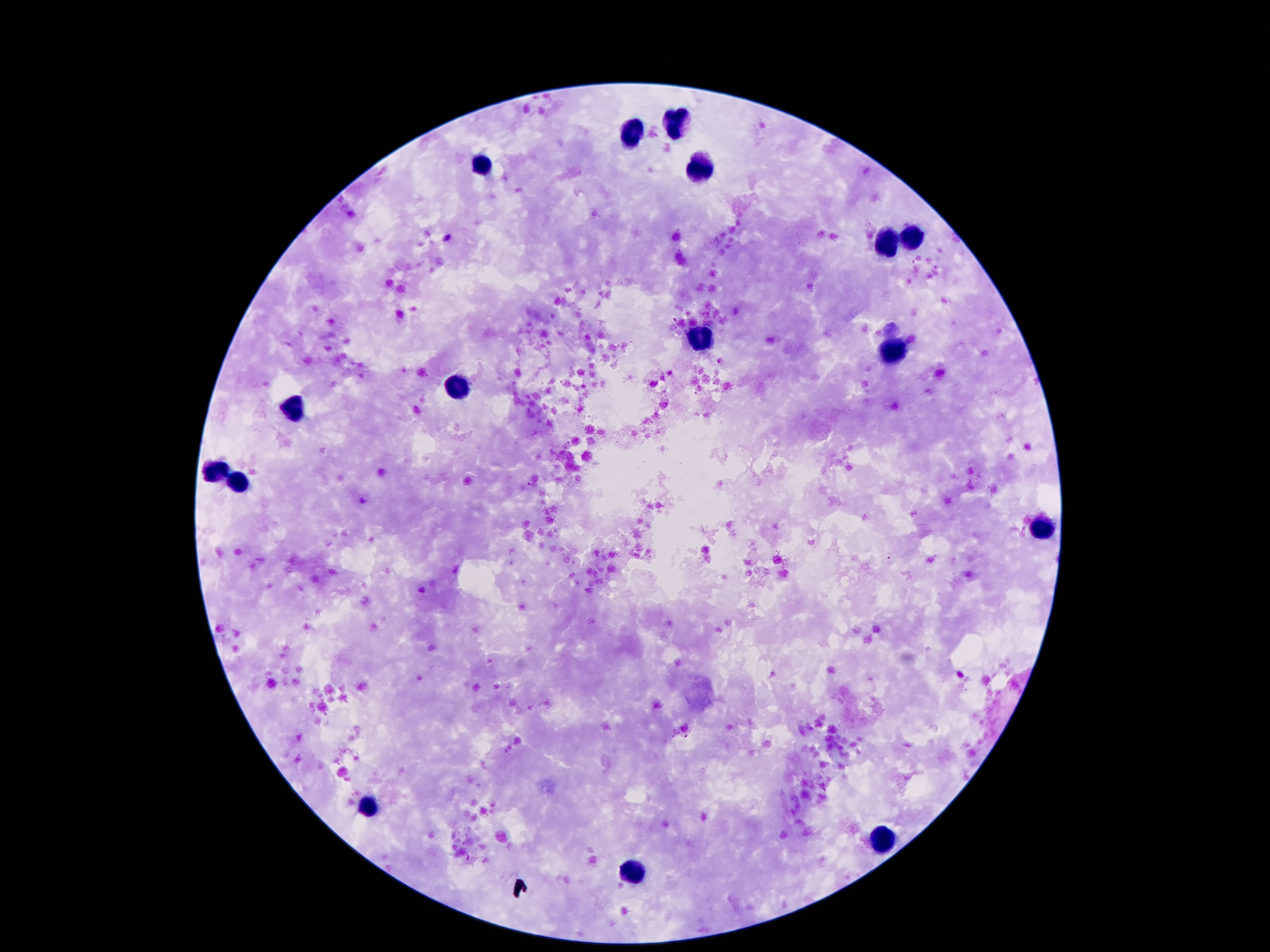
Approximate object centers, in pixels from the top-left corner.
Summary:
  - Leukocyte locations: (x=677, y=122), (x=632, y=135), (x=697, y=167), (x=481, y=169), (x=914, y=238), (x=886, y=245), (x=699, y=339), (x=891, y=353), (x=455, y=388), (x=294, y=411), (x=216, y=470), (x=236, y=482), (x=1042, y=529), (x=369, y=803), (x=880, y=839), (x=630, y=873)
  - Patient malaria status: negative
  - Capture: smartphone camera through the microscope eyepiece
  - Stain: Giemsa
  - Image size: 1270×952 pixels
  - Field of view: single
  - Magnification: 100x
  - Preparation: thick blood smear